Assess the morphology of the erythrocytes.
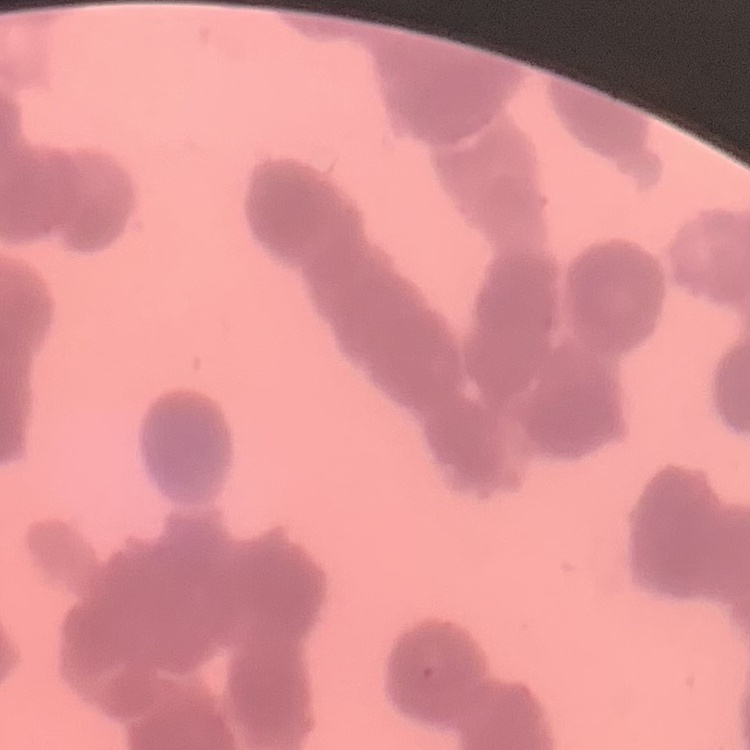

Rouleaux formation.

One tile cut from a larger photomicrograph. Field's or Giemsa stain. Thin peripheral smear.